Report the malaria status of this cell.
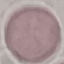

It is uninfected.

Summary:
  - Preparation: thin blood smear
  - Image type: automatically extracted cell patch, resized to 64 × 64 pixels
  - Capture: smartphone through the microscope eyepiece
  - Stain: Giemsa